Name the cell type shown.
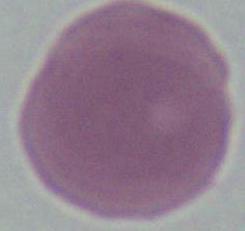

This is an erythrocyte.

Photomicrograph. 1000x magnification.